State which parasite is depicted.
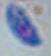

Toxoplasma gondii.

modality = photomicrograph
magnification = 1000x